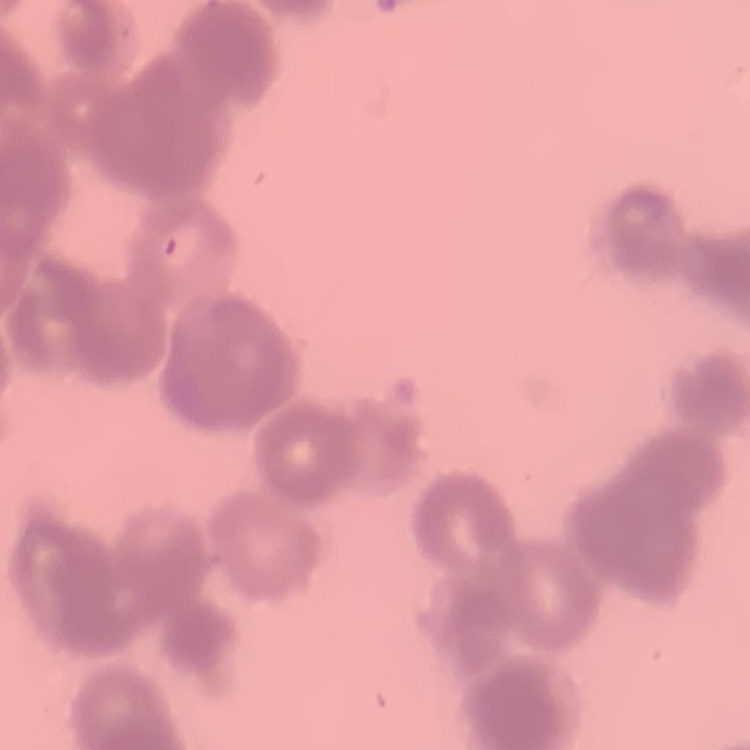 The erythrocytes show rouleaux formation. Thin peripheral smear. Square crop of a larger photomicrograph. Stained with either Field's or Giemsa.